Outline every malaria parasite.
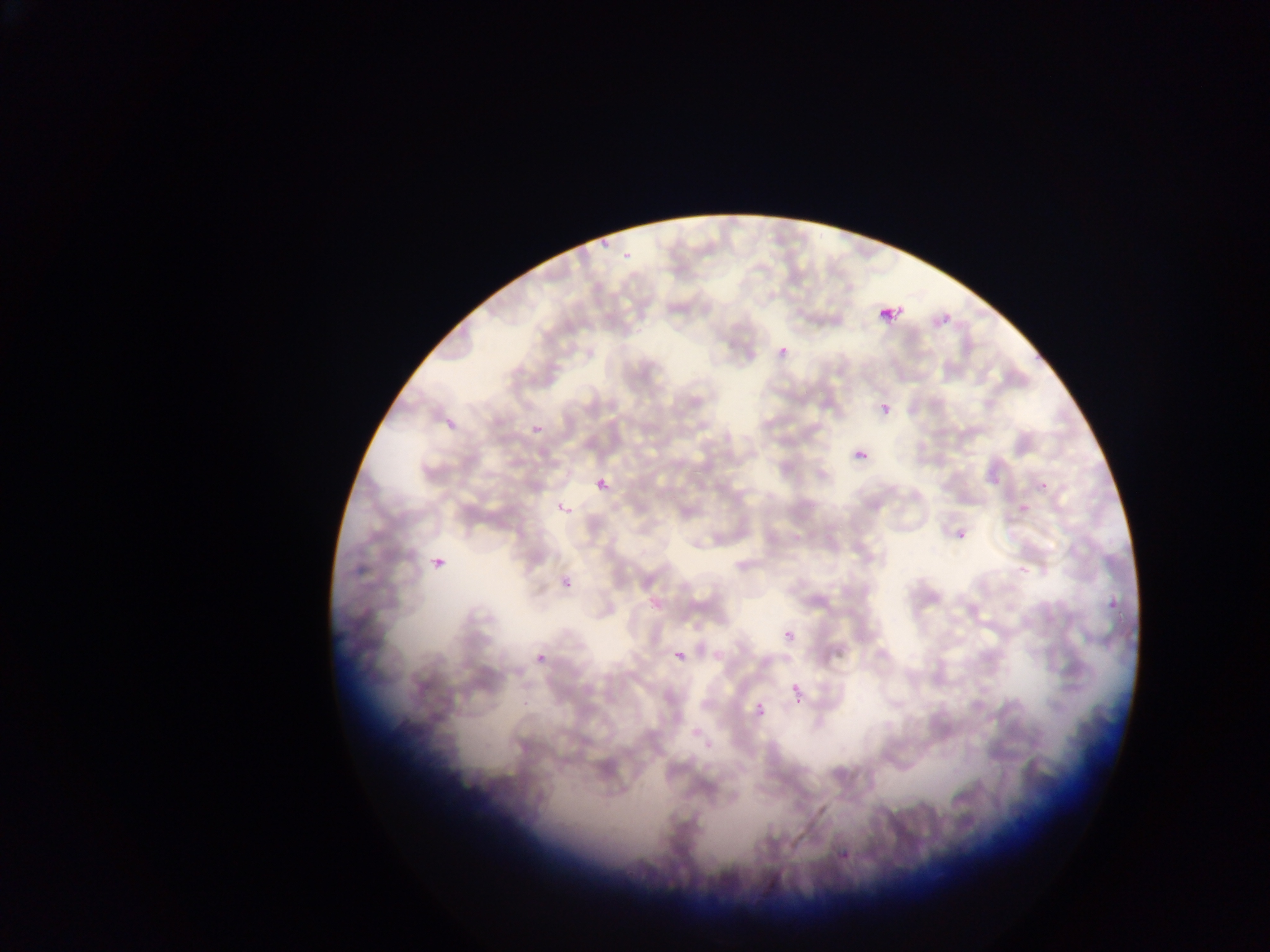
Approximate bounding boxes as [left, top, right, bottom] in pixels.
Malaria parasites: [599, 239, 610, 248], [621, 250, 635, 265], [880, 301, 906, 325], [777, 344, 791, 360], [879, 402, 891, 415], [442, 415, 463, 435], [530, 422, 547, 442], [854, 448, 871, 466], [594, 477, 611, 494], [1038, 479, 1052, 493], [558, 502, 575, 520], [950, 522, 975, 550], [430, 551, 451, 576], [557, 569, 578, 592], [1101, 591, 1124, 619], [782, 628, 797, 646], [672, 646, 691, 669], [523, 651, 551, 671], [793, 684, 803, 696], [522, 694, 537, 710], [754, 698, 765, 709], [793, 698, 804, 704], [839, 850, 849, 861] | approximate [x, y] pixel centers of objects too small to bound: [759, 716].

capture = mobile-phone photograph through a microscope
field of view = single
image size = 1270×952 pixels
preparation = thin blood smear
country = Ghana